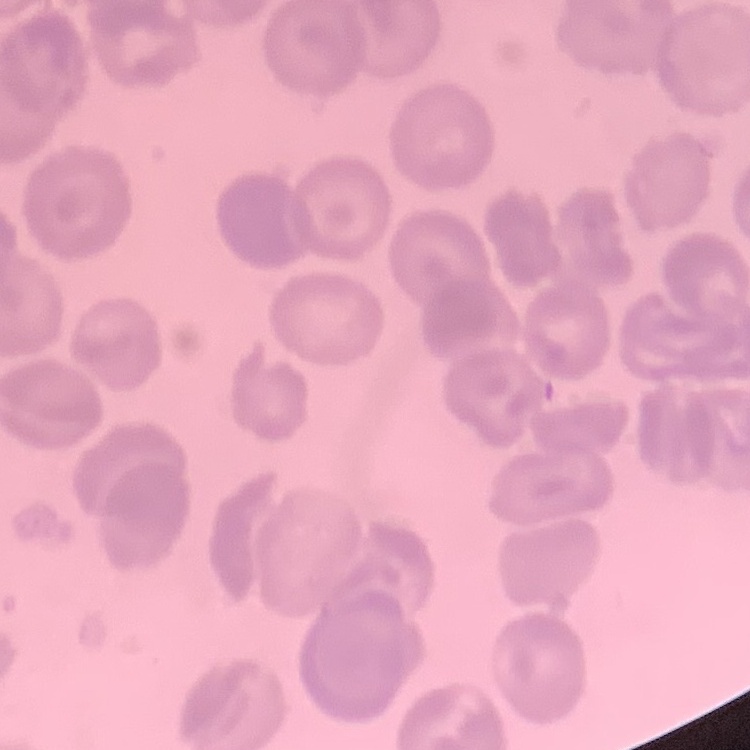
Summary:
  - Erythrocyte morphology: no rouleaux formation
  - Preparation: thin peripheral smear
  - Stain: Field's or Giemsa
  - Image type: square crop of a larger photomicrograph